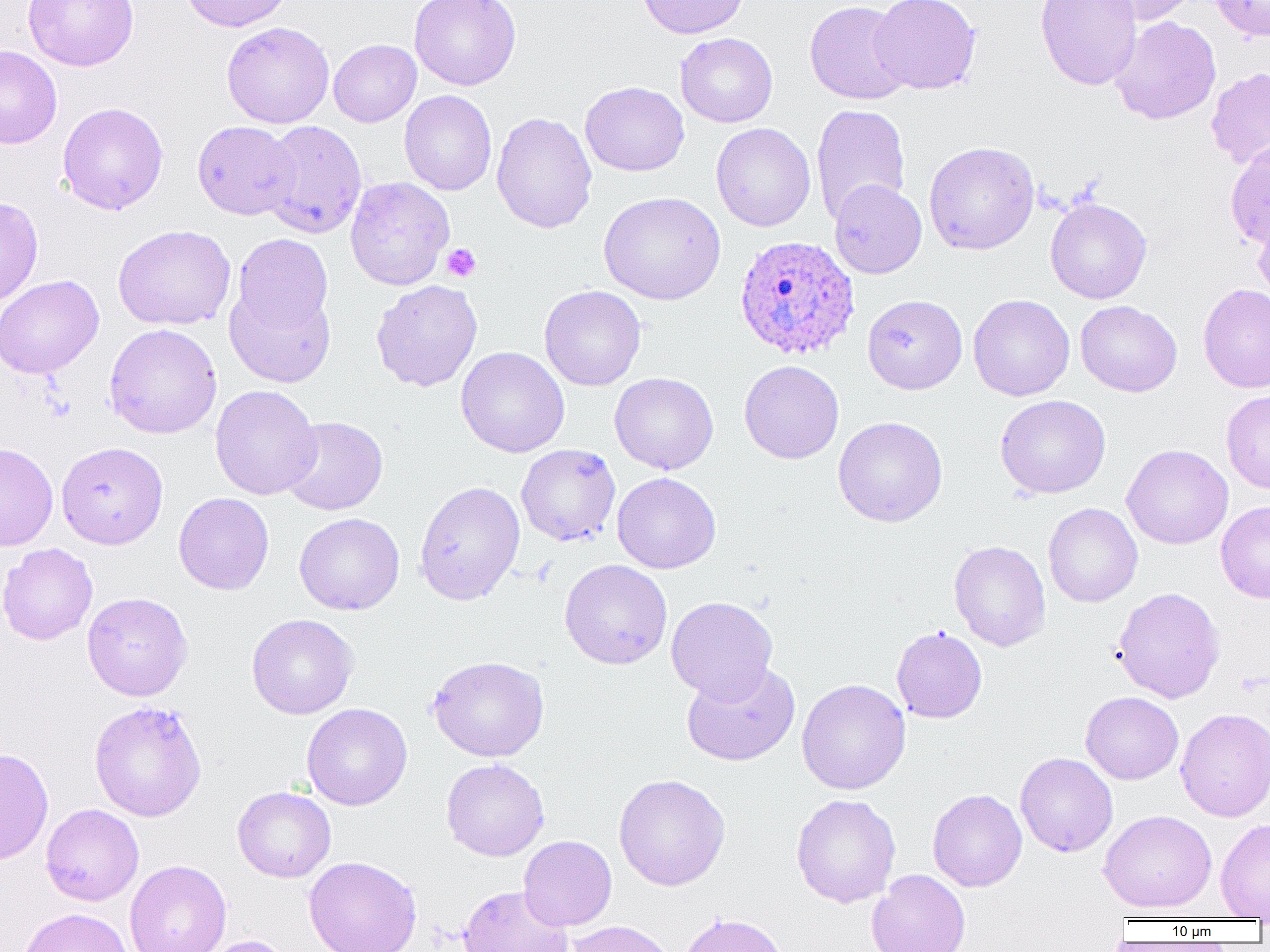
Approximate bounding boxes as [x1, y1, x2, y2] in pixels. Plasmodium ovale-infected red blood cell locations: [734, 235, 860, 360]. Platelet locations: [441, 243, 481, 282]. Uninfected red blood cell locations: [22, 0, 139, 71], [179, 0, 293, 32], [409, 0, 521, 91], [637, 0, 750, 39], [868, 0, 982, 95], [1035, 0, 1142, 91], [1094, 0, 1202, 25], [1208, 0, 1270, 42], [804, 1, 913, 105], [1109, 16, 1221, 124], [221, 22, 334, 128], [675, 32, 778, 127], [329, 39, 421, 127], [0, 45, 62, 149], [1206, 67, 1270, 169], [580, 81, 689, 176], [399, 90, 497, 196], [57, 102, 169, 214], [811, 103, 911, 224], [491, 112, 597, 233], [192, 120, 299, 220], [259, 120, 367, 238], [711, 122, 815, 232], [1225, 140, 1270, 248], [924, 141, 1039, 255], [345, 177, 455, 291], [829, 180, 927, 278], [598, 191, 725, 304], [0, 196, 43, 307], [1045, 197, 1152, 304], [1252, 207, 1270, 303], [113, 224, 236, 331], [232, 233, 334, 336], [0, 275, 104, 378], [371, 280, 482, 392], [225, 282, 336, 388], [1198, 283, 1270, 394], [540, 285, 646, 391], [863, 294, 967, 394], [968, 294, 1075, 401], [1075, 300, 1182, 396], [104, 323, 222, 439], [456, 346, 569, 457], [739, 360, 844, 463], [609, 372, 719, 474], [210, 385, 321, 500], [1221, 390, 1270, 494], [995, 394, 1111, 498], [280, 416, 388, 515], [833, 416, 948, 527], [56, 441, 168, 549], [0, 442, 58, 551], [516, 443, 620, 547], [1122, 444, 1233, 549], [612, 472, 721, 574], [414, 480, 525, 605], [173, 492, 274, 595], [1215, 500, 1270, 603], [1043, 503, 1143, 607], [294, 512, 405, 615], [949, 540, 1051, 651], [0, 542, 98, 645], [559, 559, 672, 669], [1112, 586, 1225, 703], [82, 591, 193, 701], [666, 596, 778, 703], [246, 613, 359, 719], [891, 626, 987, 723], [427, 655, 549, 762], [681, 662, 801, 766], [797, 678, 911, 795], [1081, 691, 1184, 784], [89, 700, 207, 822], [301, 703, 412, 810], [1176, 707, 1270, 821], [0, 747, 54, 866], [1015, 752, 1118, 857], [441, 758, 549, 861], [613, 773, 730, 890], [232, 786, 336, 882], [927, 789, 1027, 891], [791, 793, 901, 907], [41, 804, 144, 906], [1098, 809, 1217, 913], [1215, 818, 1270, 920], [519, 835, 617, 930], [304, 856, 422, 952], [125, 859, 231, 952], [866, 869, 971, 952], [458, 885, 574, 952], [18, 907, 133, 952], [678, 912, 789, 952], [564, 920, 677, 952], [198, 935, 296, 952]. Slide-level diagnosis: Plasmodium ovale. Optical microscopy. Image is 1270×952 pixels. 1000x magnification. Thin blood film. One field of a larger specimen.